Identify the cell.
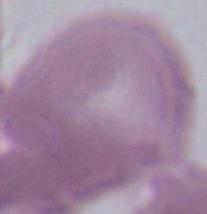

An erythrocyte.

Captured at 1000x magnification. Photomicrograph.